Locate every malaria parasite and every leukocyte.
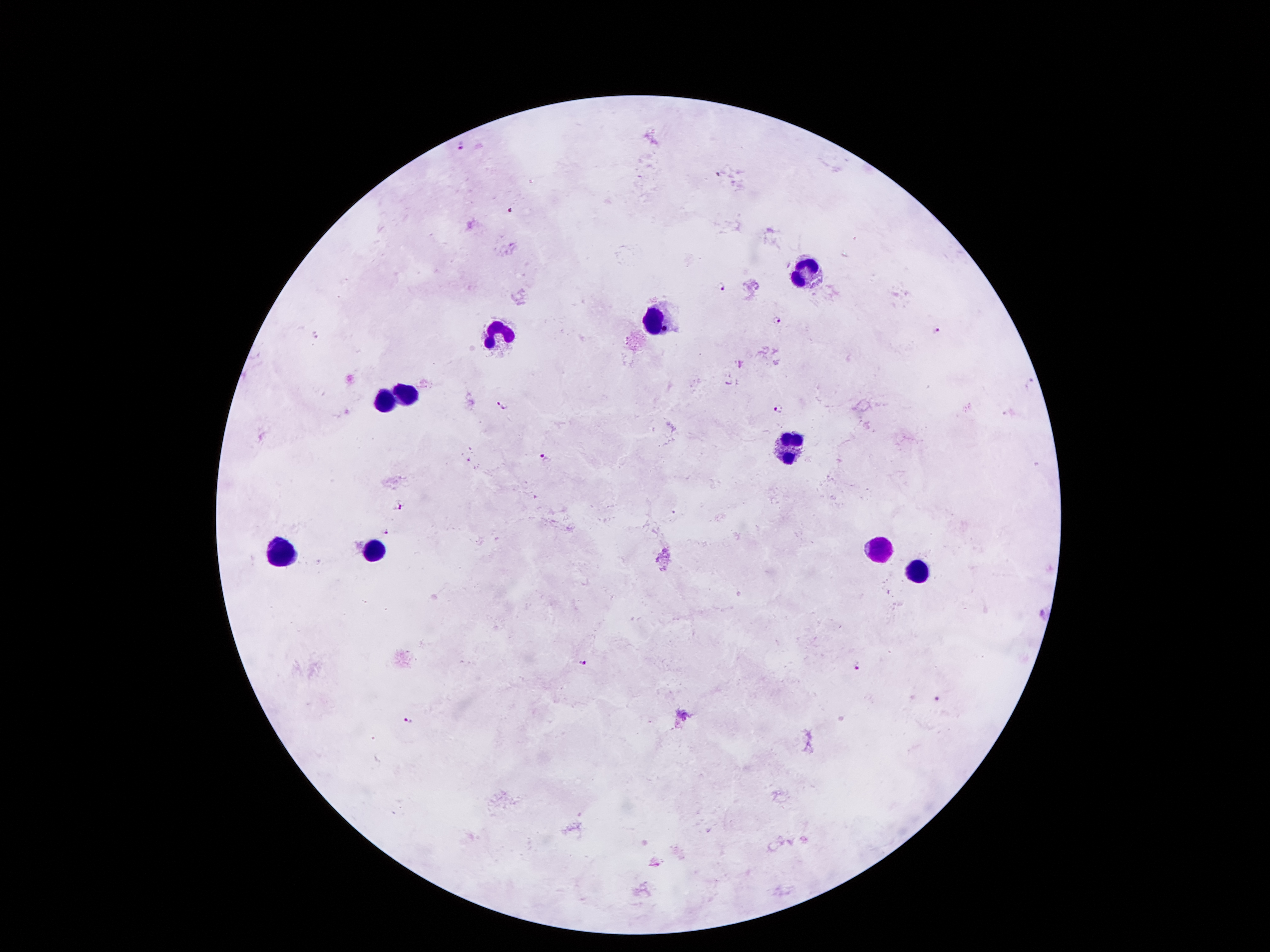

Approximate centers as [x, y] in pixels.
Malaria parasites: [462, 143], [721, 173], [510, 208], [724, 290], [778, 321], [936, 331], [503, 405], [777, 408], [543, 458], [398, 506], [675, 512], [386, 532], [1044, 614], [582, 660], [857, 668], [938, 700], [412, 719].
Leukocytes: [804, 272], [652, 321], [494, 334], [405, 393], [385, 403], [794, 448], [873, 546], [378, 550], [280, 552], [922, 574].

magnification = 100x
capture = smartphone camera through the microscope eyepiece
field of view = one from this slide
image size = 1270×952 pixels
patient malaria status = infected with Plasmodium falciparum
stain = Giemsa
preparation = thick peripheral-blood smear